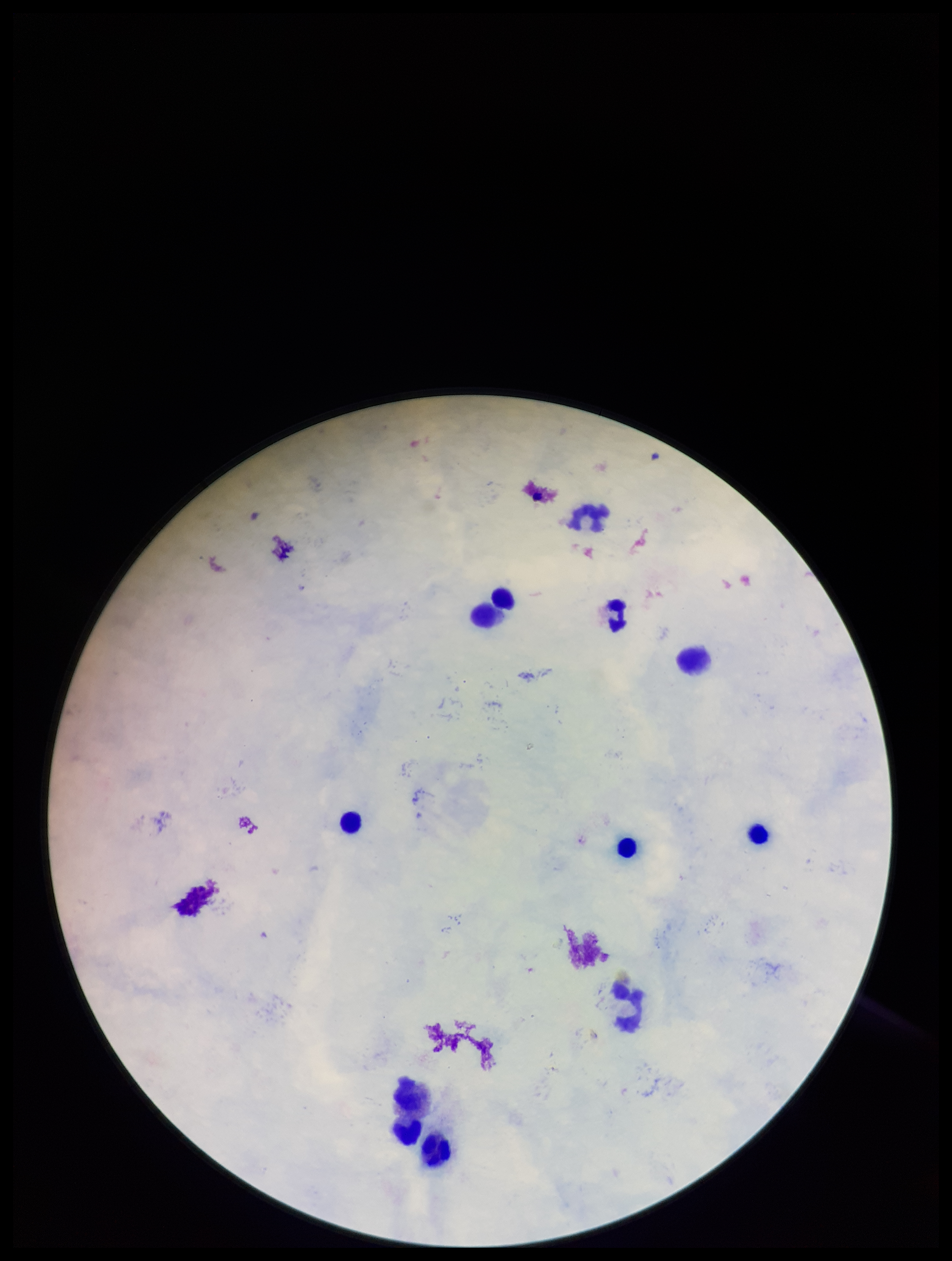 Preparation: thick blood smear. Parasite count: 0. Plasmodium parasites: none detected. Stained with Giemsa. Photographed through the microscope eyepiece with a smartphone camera. Image is 952×1261 pixels. Single field of view. Leukocyte count: 10. Patient malaria status: negative.